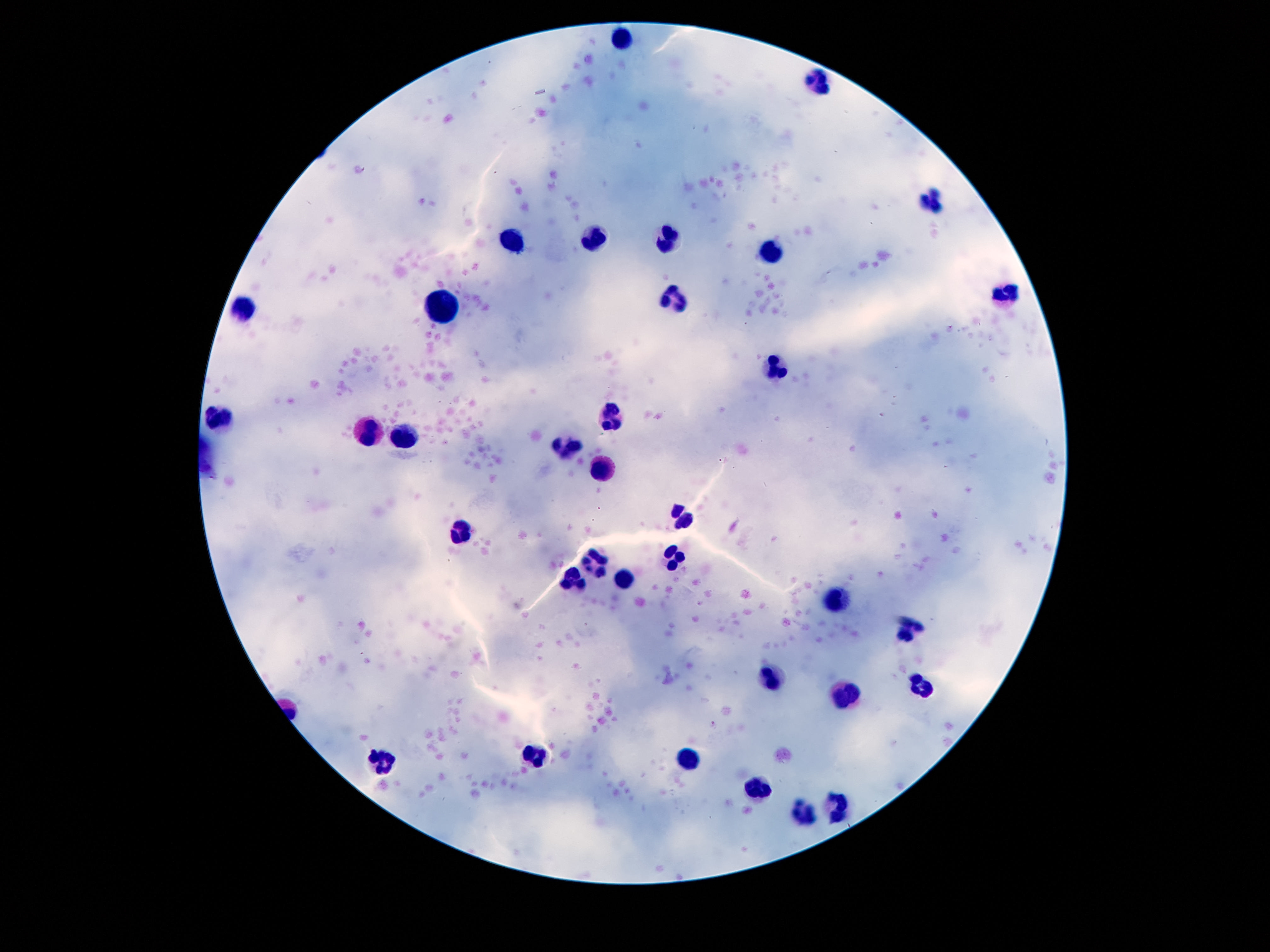
Approximate centers as (x, y) in pixels.
Summary:
  - Leukocyte locations: (625, 40), (819, 84), (934, 202), (592, 235), (670, 237), (514, 240), (772, 254), (1004, 296), (672, 301), (444, 307), (244, 310), (776, 366), (612, 414), (219, 416), (369, 432), (404, 439), (567, 448), (602, 471), (682, 518), (461, 532), (672, 556), (592, 560), (623, 579), (572, 581), (836, 597), (910, 628), (770, 676), (918, 683), (848, 693), (535, 753), (690, 758), (383, 763), (760, 790), (838, 808), (801, 810)
  - Preparation: thick peripheral-blood smear
  - Field of view: one from this slide
  - Image size: 1270×952 pixels
  - Patient malaria status: uninfected
  - Magnification: 100x
  - Stain: Giemsa
  - Capture: smartphone camera through the microscope eyepiece